Assess this cell for malaria.
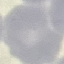
Uninfected.

Giemsa stain. Photographed with a smartphone camera at the microscope eyepiece. Automatically extracted cell patch, resized to 64 × 64 pixels. Thin smear of blood.